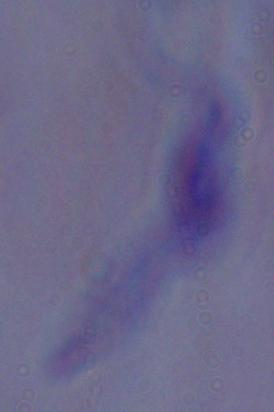
identification: trypanosome
modality: photomicrograph
magnification: 1000x